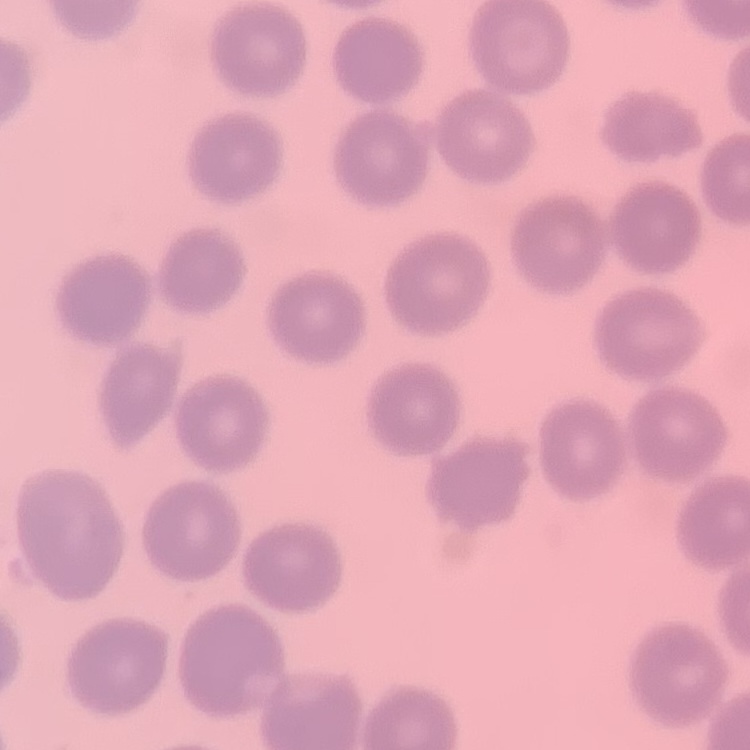
Summary:
  - Red blood cell morphology: no rouleaux formation
  - Preparation: thin blood smear
  - Image type: one tile cut from a larger photomicrograph
  - Stain: Field's or Giemsa